Report the malaria status of this cell.
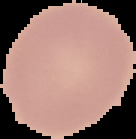

It is uninfected.

Summary:
  - Preparation: thin blood film
  - Image type: segmented cell region on a black background
  - Image size: 136×139 pixels